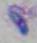
Toxoplasma gondii is shown. Captured at 1000x magnification. Micrograph.